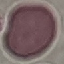
Result: negative for malaria parasites. Thin smear of blood. Giemsa-stained preparation. Cell patch, automatically extracted from a larger field of view and resized to 64 × 64 pixels. Acquired by smartphone through the microscope eyepiece.